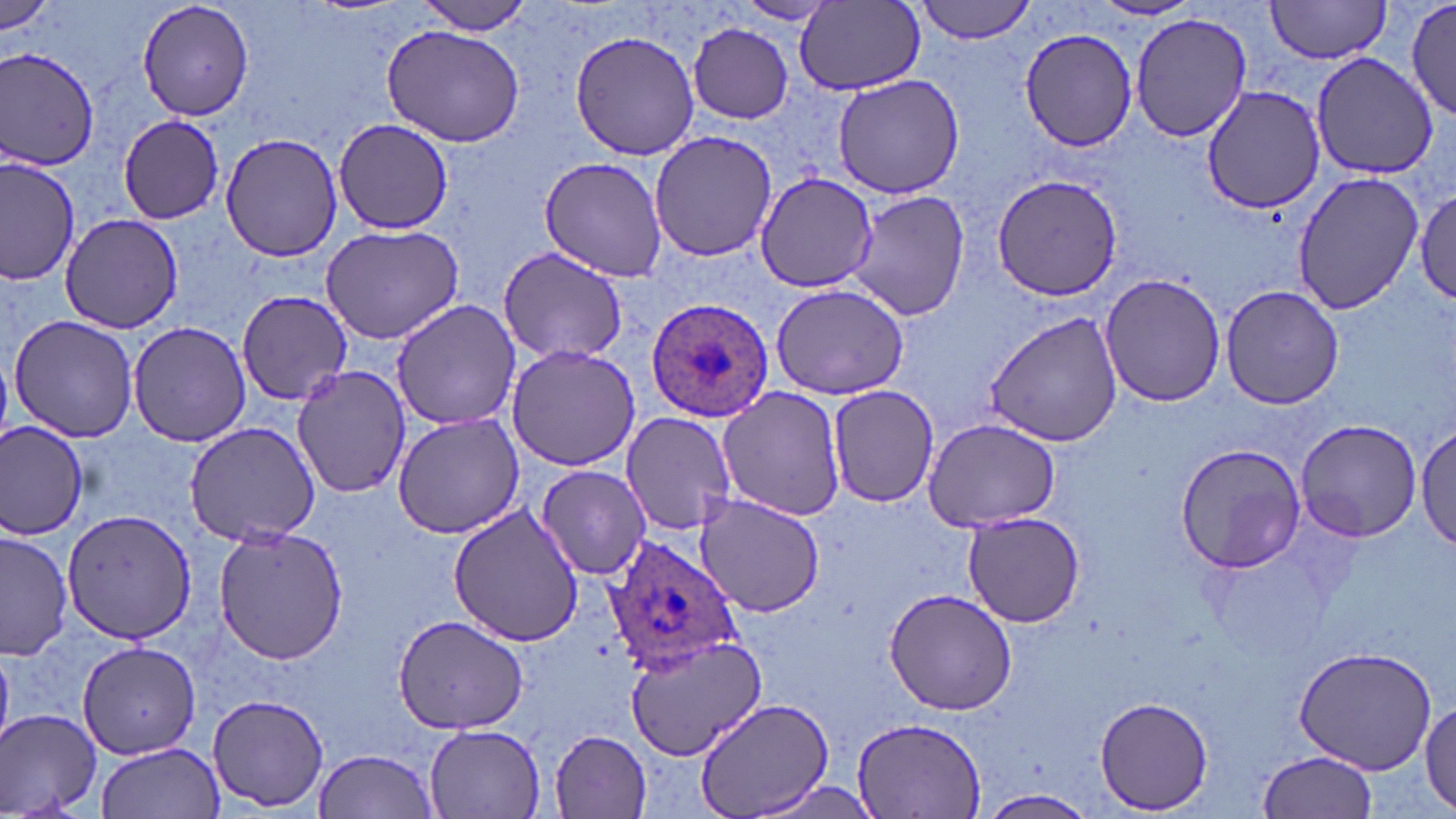

Summary:
  - Coordinate format: approximate bounding boxes as (x1, y1, x2, y2) in pixels
  - Plasmodium ovale-infected red blood cell locations: (647, 298, 774, 422), (605, 537, 742, 674)
  - Uninfected red blood cell locations: (134, 0, 256, 121), (914, 0, 1038, 43), (1265, 0, 1394, 63), (1409, 0, 1454, 123), (796, 1, 926, 94), (0, 2, 57, 38), (409, 2, 537, 35), (732, 2, 838, 26), (1130, 13, 1251, 141), (688, 22, 794, 124), (380, 23, 525, 148), (567, 28, 700, 160), (1019, 28, 1137, 153), (1, 46, 99, 170), (1308, 53, 1435, 179), (831, 73, 963, 200), (1200, 85, 1325, 212), (116, 113, 225, 224), (335, 121, 454, 234), (648, 129, 777, 265), (220, 132, 342, 263), (1, 153, 79, 287), (538, 156, 671, 281), (1289, 170, 1422, 314), (753, 172, 880, 292), (991, 174, 1126, 300), (1412, 182, 1455, 309), (844, 189, 969, 322), (60, 213, 186, 333), (318, 226, 464, 346), (498, 248, 631, 365), (1100, 273, 1225, 409), (770, 284, 911, 400), (1220, 285, 1345, 410), (234, 289, 352, 405), (392, 299, 523, 430), (985, 310, 1123, 448), (8, 315, 139, 443), (128, 321, 253, 447), (504, 343, 641, 471), (292, 366, 407, 501), (827, 384, 939, 508), (716, 387, 846, 522), (619, 411, 738, 536), (392, 412, 524, 538), (1295, 418, 1423, 541), (1416, 419, 1454, 555), (922, 420, 1059, 531), (0, 422, 88, 538), (182, 422, 323, 545), (1176, 444, 1307, 573), (535, 463, 652, 580), (692, 494, 826, 618), (447, 506, 587, 650), (63, 511, 195, 645), (961, 511, 1085, 628), (212, 526, 348, 665), (1, 529, 74, 662), (883, 588, 1021, 717), (391, 613, 531, 735), (625, 635, 767, 758), (77, 640, 201, 758), (1292, 645, 1438, 773), (206, 693, 330, 812), (1094, 696, 1213, 814), (695, 698, 834, 819), (1420, 700, 1456, 813), (0, 708, 106, 818), (850, 718, 988, 816), (422, 723, 547, 817), (551, 731, 651, 816), (96, 741, 224, 819), (313, 748, 441, 818), (1255, 750, 1378, 818), (743, 777, 886, 818), (980, 789, 1099, 819)
  - Slide-level diagnosis: Plasmodium ovale
  - Stain: May-Grünwald-Giemsa
  - Magnification: 1000x
  - Modality: optical microscopy
  - Image size: 1456×819 pixels
  - Field of view: single
  - Preparation: thin blood film